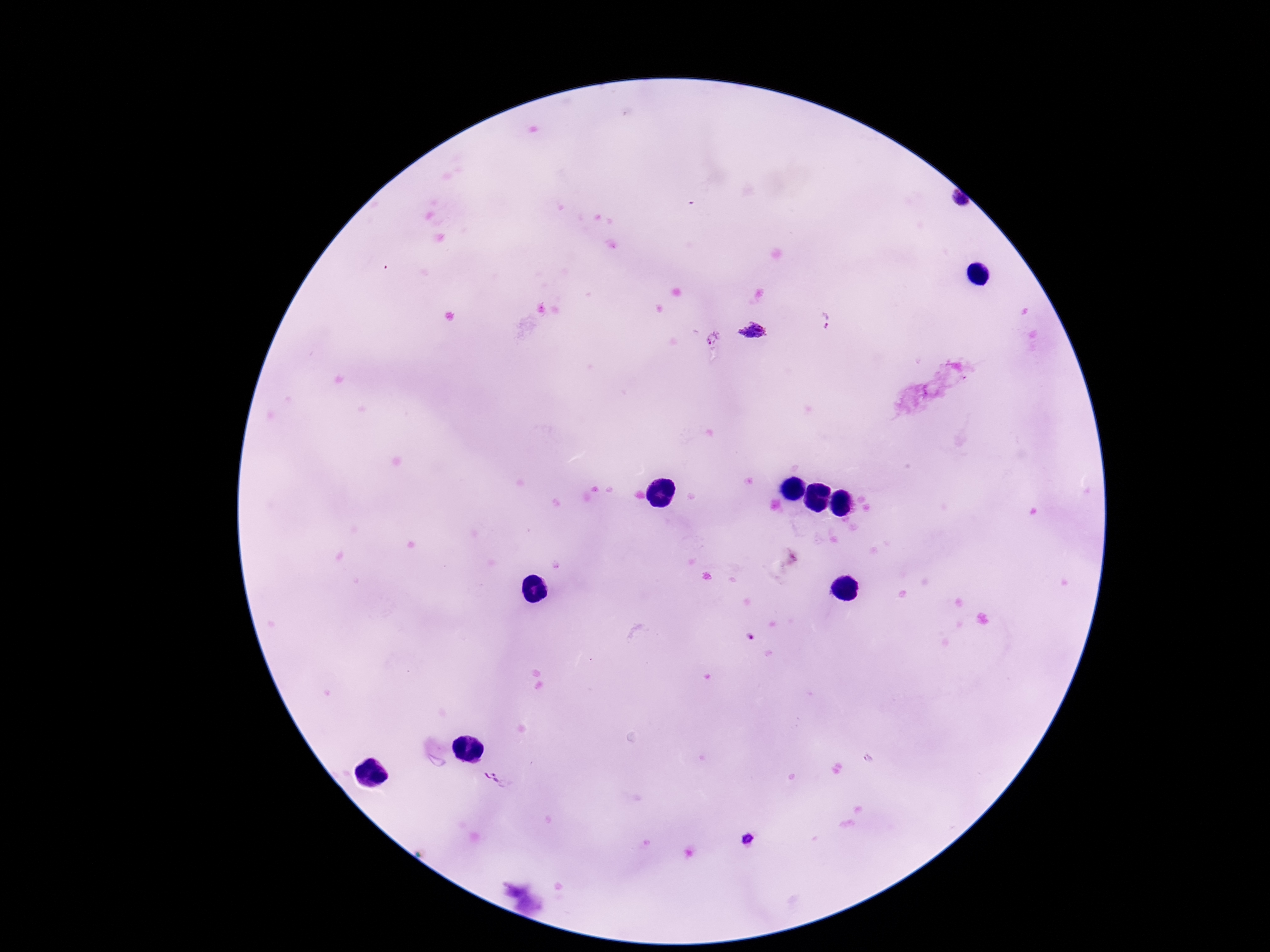

{
  "plasmodium_parasite_locations": "approximate centers as (x, y) in pixels: (824, 321), (755, 335), (712, 337)",
  "magnification": "100x",
  "field_of_view": "single",
  "stain": "Giemsa",
  "capture": "smartphone camera through the microscope eyepiece",
  "image_size": "1270×952 pixels",
  "preparation": "thick blood film",
  "patient_malaria_status": "infected"
}